Assess the morphology of the red blood cells.
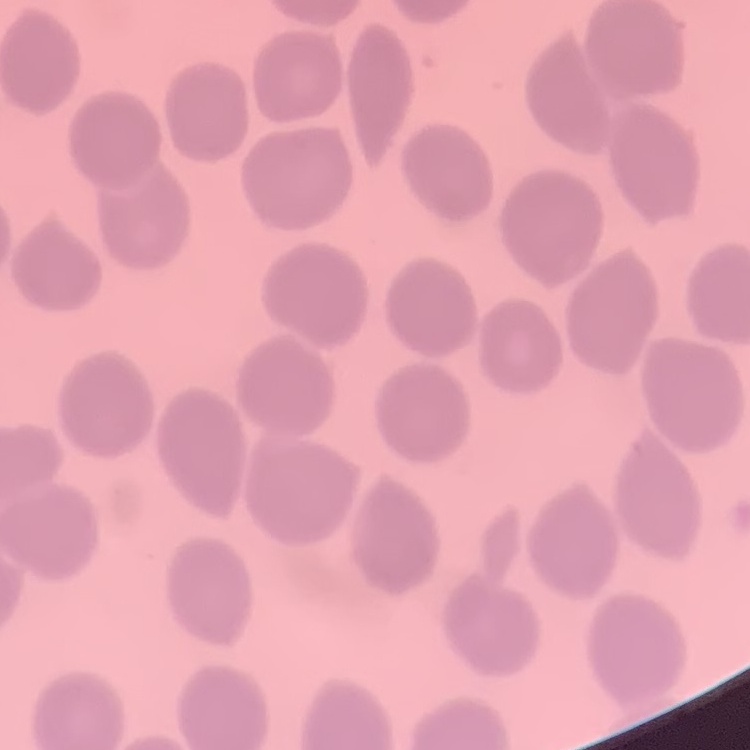
They show no rouleaux formation.

One tile cut from a larger photomicrograph. Thin blood smear. Field's or Giemsa stain.